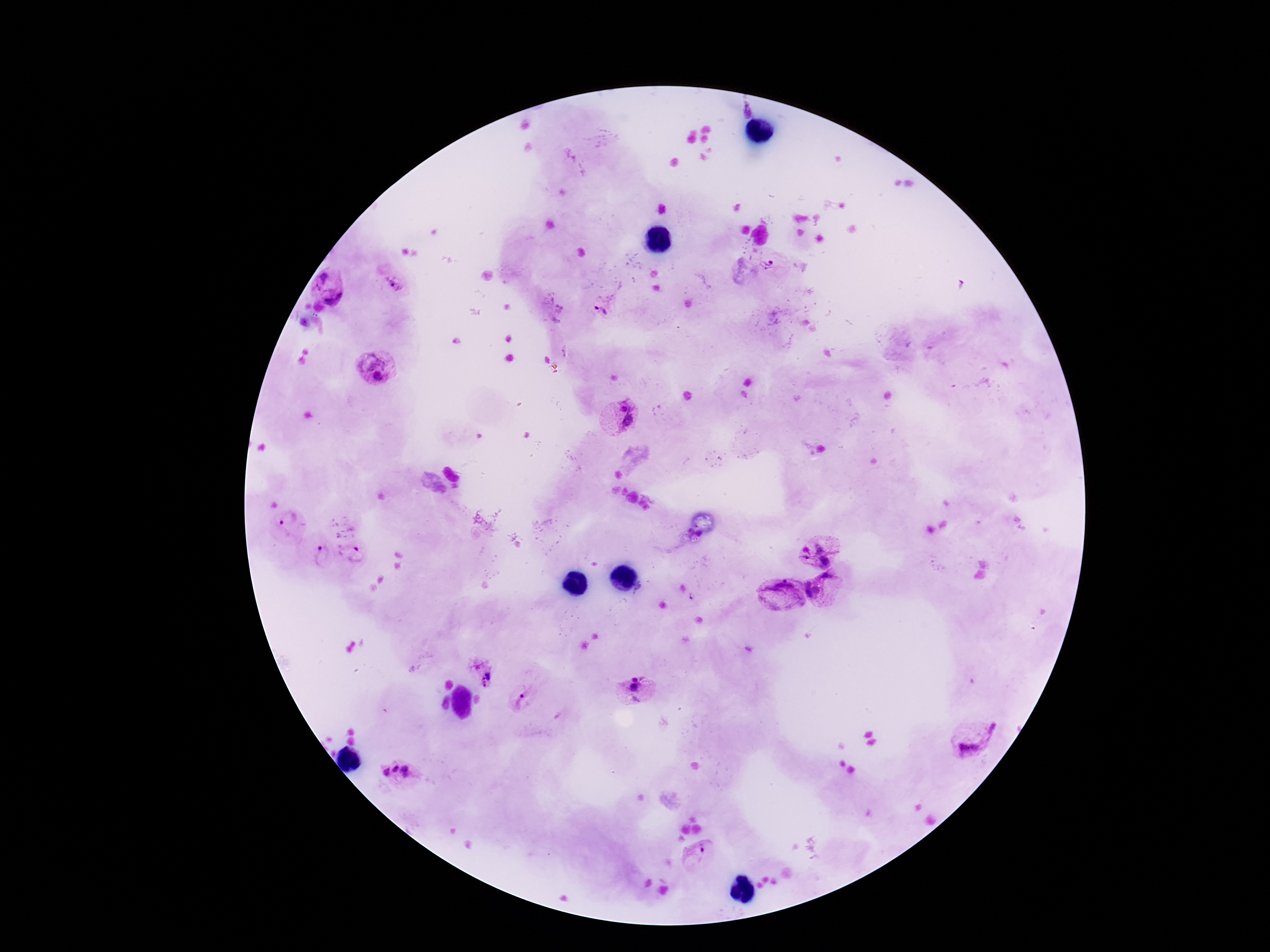 Approximate centers as {x, y} in pixels. Plasmodium parasite locations: {746, 109}, {755, 270}, {329, 286}, {396, 286}, {609, 302}, {554, 305}, {376, 364}, {618, 417}, {286, 524}, {821, 546}, {353, 552}, {322, 554}, {827, 588}, {782, 594}, {482, 670}, {638, 691}, {526, 699}, {973, 739}, {401, 773}, {697, 855}. Giemsa stain. Patient malaria status: infected. One field from this slide. Photographed through the microscope eyepiece with a smartphone camera. Image is 1270×952 pixels. 100x magnification. Thick blood film.